Point out each leukocyte.
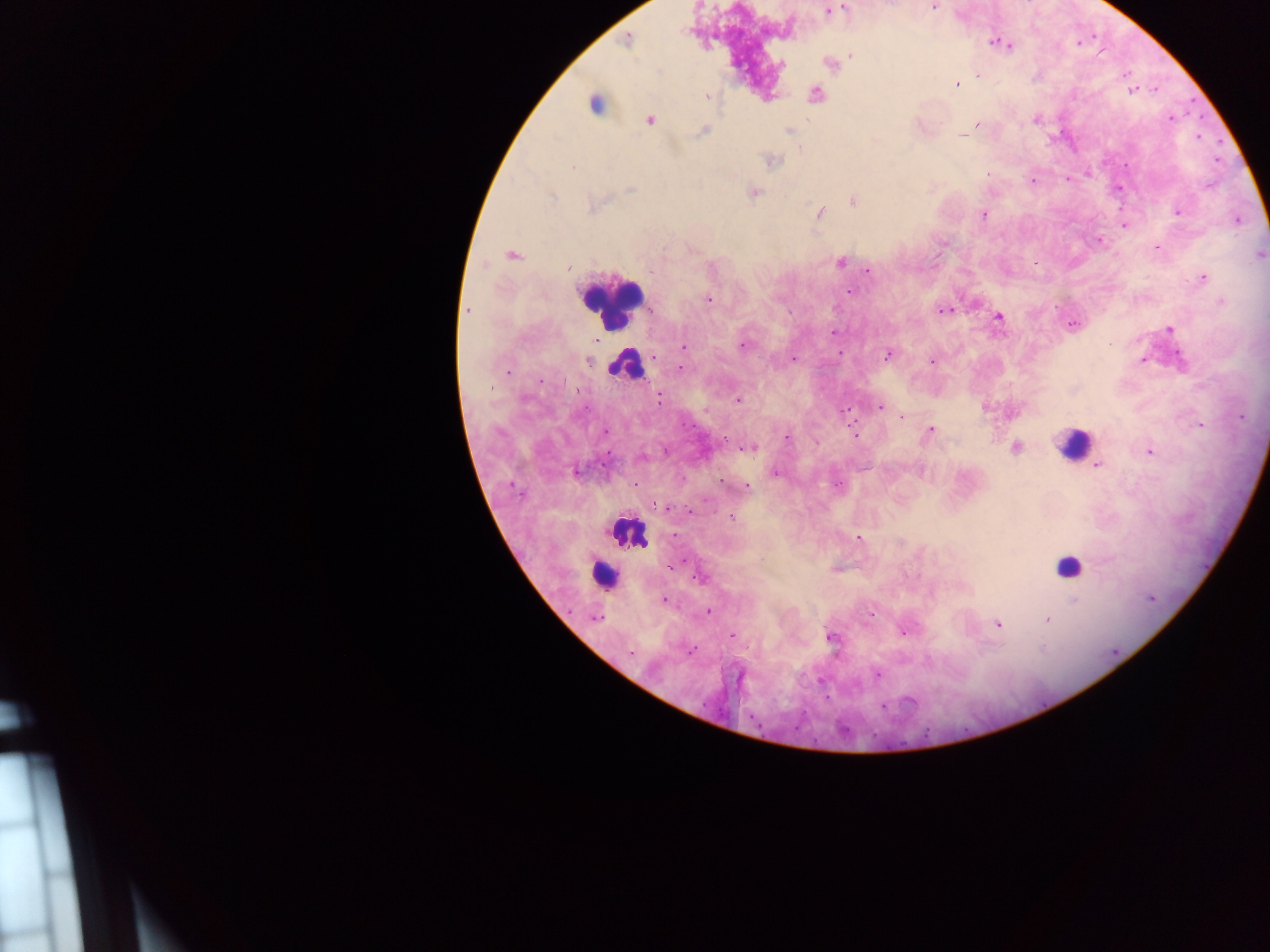

Approximate centers as (x, y) in pixels.
Leukocytes: (599, 107), (610, 301), (626, 364), (1073, 443), (628, 531), (1069, 568), (602, 575).

Summary:
  - Plasmodium parasite locations: (933, 7), (845, 9), (829, 11), (628, 39), (1077, 42), (995, 43), (1003, 43), (1008, 45), (851, 55), (830, 64), (977, 74), (1125, 74), (956, 85), (1131, 89), (1156, 89), (815, 94), (707, 96), (1171, 117), (1036, 119), (649, 120), (976, 125), (703, 130), (789, 131), (962, 136), (1197, 137), (771, 160), (573, 167), (987, 173), (1067, 179), (1032, 180), (1117, 188), (753, 193), (853, 201), (1177, 211), (819, 212), (983, 214), (1237, 220), (1123, 224), (1099, 241), (1157, 248), (1259, 254), (511, 255), (840, 262), (568, 266), (867, 270), (1202, 277), (850, 291), (707, 299), (1221, 301), (467, 311), (943, 311), (998, 317), (1072, 324), (1169, 328), (833, 332), (743, 344), (684, 346), (888, 355), (793, 358), (589, 359), (931, 360), (1143, 360), (680, 368), (506, 372), (738, 399), (660, 400), (878, 406), (985, 407), (844, 410), (1013, 412), (901, 416), (1200, 424), (930, 430), (603, 432), (855, 434), (787, 437), (748, 447), (1015, 447), (1149, 452), (640, 457), (1096, 465), (576, 470), (775, 472), (722, 481), (837, 485), (746, 486), (730, 516), (673, 536), (859, 537), (836, 569), (699, 577), (1151, 598), (663, 600), (708, 611), (870, 613), (596, 617), (1047, 619), (997, 623), (903, 629), (732, 635), (831, 637), (689, 651), (876, 674)
  - Country: Ghana
  - Capture: mobile-phone photograph through a microscope
  - Field of view: single
  - Preparation: thick blood smear
  - Image size: 1270×952 pixels